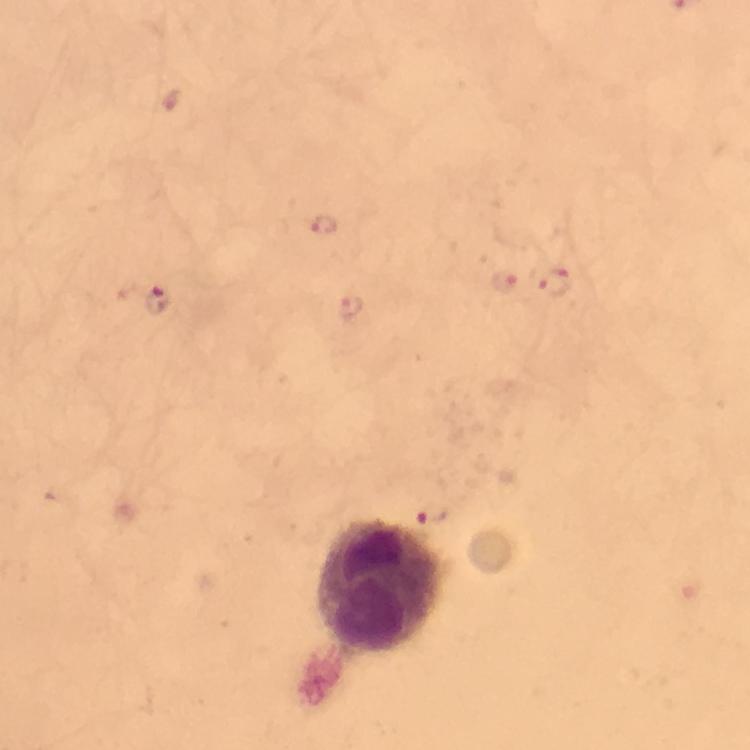

Approximate centers as [x, y] in pixels.
Summary:
  - Leukocyte locations: [377, 586]
  - Plasmodium parasite locations: [324, 224], [503, 281], [553, 282], [158, 299], [348, 304], [433, 518]
  - Immersion oil: applied
  - Cropped from: a single field of view
  - Magnification: 100x
  - Preparation: thick blood smear
  - Stain: Giemsa
  - Context: from a malaria diagnostic workup
  - Capture: smartphone mounted on the microscope
  - Image size: 750×750 pixels